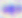

400x magnification. Photomicrograph. Toxoplasma gondii is seen.